Assess this cell for malaria.
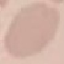
It is uninfected.

preparation: thin blood smear
stain: Giemsa
image_type: cell patch, automatically extracted from a larger field of view and resized to 64 × 64 pixels
capture: smartphone through the microscope eyepiece